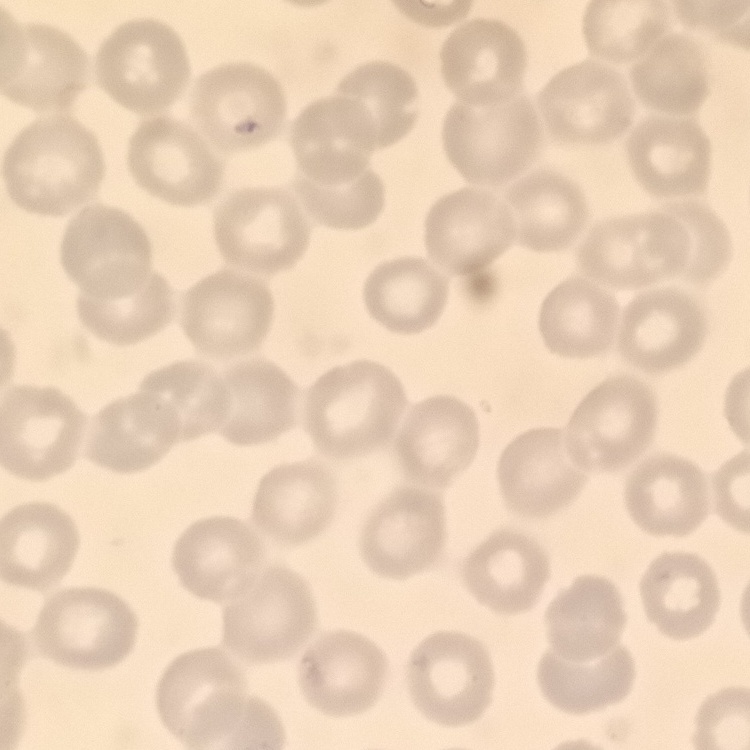
red_blood_cell_morphology: no rouleaux formation
image_type: square crop of a larger photomicrograph
stain: Field's or Giemsa
preparation: thin blood film